Identify the blood parasite species.
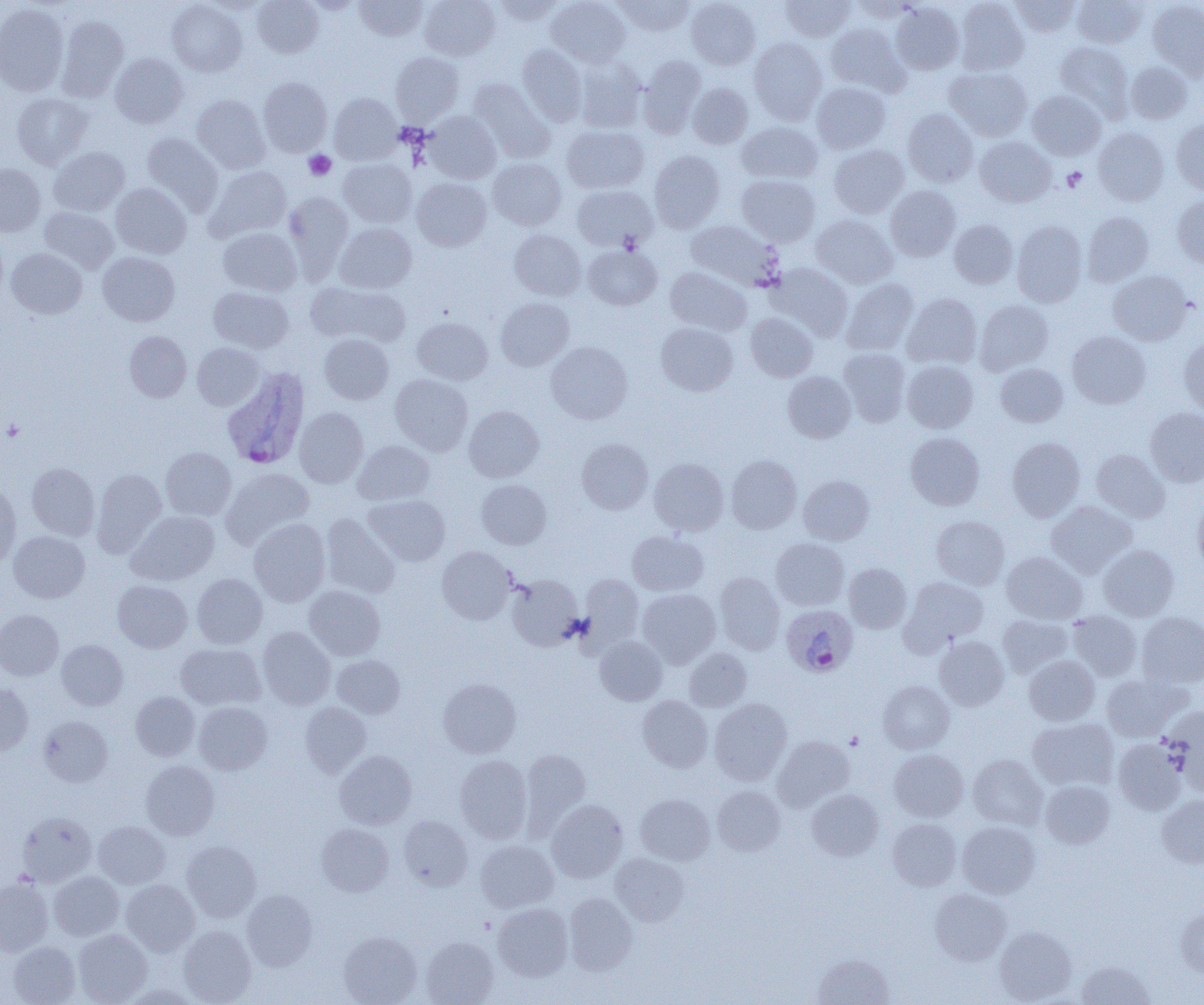

Plasmodium ovale.

Summary:
  - Coordinate format: approximate bounding boxes as (x1, y1, x2, y2) in pixels
  - Uninfected red blood cell locations: (203, 0, 270, 16), (252, 0, 323, 58), (303, 0, 362, 14), (354, 0, 428, 41), (420, 0, 499, 60), (492, 0, 568, 25), (546, 0, 631, 67), (614, 0, 695, 36), (686, 0, 760, 70), (779, 0, 856, 42), (954, 0, 1029, 75), (1010, 0, 1082, 37), (1146, 0, 1204, 79), (167, 1, 247, 77), (1072, 1, 1146, 48), (0, 3, 68, 95), (890, 3, 965, 75), (56, 16, 129, 101), (825, 23, 908, 96), (749, 37, 827, 125), (1054, 42, 1134, 120), (517, 44, 588, 126), (390, 51, 463, 124), (110, 53, 189, 128), (638, 55, 706, 137), (574, 57, 647, 133), (1125, 60, 1193, 124), (944, 66, 1033, 141), (258, 77, 332, 157), (467, 78, 555, 163), (812, 82, 891, 154), (687, 83, 753, 149), (1027, 90, 1106, 160), (329, 92, 401, 165), (11, 93, 91, 169), (191, 94, 270, 173), (903, 108, 978, 187), (425, 111, 501, 184), (1171, 117, 1204, 195), (737, 122, 823, 184), (562, 125, 649, 193), (1093, 127, 1169, 206), (140, 133, 223, 216), (975, 136, 1056, 207), (829, 144, 909, 218), (49, 146, 130, 216), (649, 150, 725, 232), (338, 158, 416, 227), (488, 158, 566, 230), (0, 164, 45, 237), (204, 166, 291, 243), (737, 174, 820, 246), (412, 178, 491, 251), (111, 183, 191, 258), (572, 185, 657, 251), (886, 185, 961, 261), (283, 192, 354, 281), (1172, 196, 1204, 269), (39, 207, 119, 274), (1082, 211, 1154, 286), (811, 214, 898, 289), (949, 219, 1018, 288), (1011, 220, 1087, 308), (685, 221, 782, 291), (334, 223, 417, 293), (217, 227, 301, 296), (509, 229, 586, 300), (583, 244, 662, 310), (6, 248, 87, 318), (97, 252, 179, 326), (768, 263, 853, 340), (665, 267, 751, 336), (1107, 270, 1194, 345), (841, 278, 918, 356), (308, 281, 410, 348), (209, 287, 294, 353), (902, 293, 982, 369), (495, 297, 574, 370), (975, 299, 1053, 375), (746, 313, 818, 381), (412, 316, 492, 385), (656, 321, 739, 396), (124, 331, 191, 402), (1067, 331, 1151, 409), (319, 334, 394, 404), (1179, 337, 1204, 417), (546, 341, 632, 424), (192, 343, 265, 410), (839, 348, 910, 427), (902, 360, 978, 433), (995, 363, 1068, 427), (783, 371, 856, 443), (390, 373, 472, 455), (464, 406, 544, 482), (295, 407, 368, 488), (1146, 407, 1204, 487), (905, 433, 985, 510), (1007, 437, 1085, 521), (577, 439, 653, 514), (353, 440, 434, 505), (161, 447, 236, 520), (1091, 449, 1169, 522), (726, 455, 802, 534), (649, 458, 729, 536), (26, 463, 100, 540), (91, 468, 166, 557), (221, 468, 315, 548), (798, 475, 874, 545), (476, 479, 551, 549), (0, 485, 20, 569), (364, 495, 450, 566), (1192, 498, 1204, 576), (1046, 501, 1137, 578), (127, 511, 219, 585), (321, 513, 400, 598), (930, 516, 1009, 589), (249, 518, 330, 606), (9, 531, 89, 603), (627, 531, 708, 596), (771, 538, 849, 610), (1098, 544, 1179, 621), (437, 546, 515, 624), (1002, 551, 1087, 624), (844, 563, 911, 633), (714, 572, 785, 654), (192, 573, 267, 649), (507, 574, 583, 651), (579, 575, 643, 651), (902, 576, 989, 650), (113, 580, 192, 653), (304, 585, 385, 660), (638, 589, 721, 667), (0, 609, 63, 680), (1067, 610, 1142, 681), (1137, 612, 1204, 687), (998, 614, 1073, 678), (257, 626, 335, 709), (934, 636, 1009, 710), (595, 637, 667, 705), (56, 640, 128, 710), (176, 643, 266, 710), (685, 647, 752, 711), (332, 654, 405, 719), (1024, 656, 1099, 725), (1101, 673, 1190, 741), (438, 678, 521, 758), (878, 681, 954, 753), (0, 683, 33, 755), (130, 692, 200, 761), (637, 695, 713, 772), (710, 699, 792, 785), (194, 702, 272, 774), (300, 702, 371, 777), (1164, 708, 1204, 794), (38, 715, 112, 786), (1027, 717, 1118, 791), (773, 736, 854, 811), (1113, 739, 1185, 814), (520, 749, 590, 833), (890, 749, 968, 821), (335, 750, 416, 828), (455, 755, 532, 842), (968, 755, 1048, 830), (141, 760, 219, 840), (1040, 780, 1115, 848), (712, 785, 785, 856), (807, 789, 884, 861), (635, 794, 715, 865), (1156, 796, 1204, 867), (546, 799, 627, 882), (17, 812, 96, 886), (398, 815, 473, 891), (887, 818, 961, 891), (93, 820, 170, 889), (957, 822, 1041, 898), (316, 823, 393, 896), (476, 840, 559, 912), (181, 841, 261, 921), (610, 853, 689, 926), (49, 871, 124, 940), (0, 878, 52, 955), (121, 879, 199, 956), (930, 888, 1011, 965), (242, 889, 317, 971), (563, 893, 637, 976), (492, 903, 573, 981), (1176, 906, 1204, 977), (179, 926, 256, 1004), (994, 926, 1076, 1004), (74, 930, 152, 1004), (338, 931, 421, 1005), (421, 936, 499, 1005), (8, 941, 80, 1005), (813, 954, 895, 1004), (1077, 960, 1155, 1004), (120, 984, 202, 1004)
  - Plasmodium ovale-infected red blood cell locations: (221, 368, 310, 470), (781, 604, 858, 677)
  - Platelet locations: (303, 150, 336, 180), (1062, 167, 1087, 192), (2, 420, 26, 440), (846, 732, 864, 749)
  - Field of view: one of a larger specimen
  - Modality: optical microscopy
  - Preparation: thin blood smear
  - Magnification: 1000x
  - Image size: 1204×1005 pixels